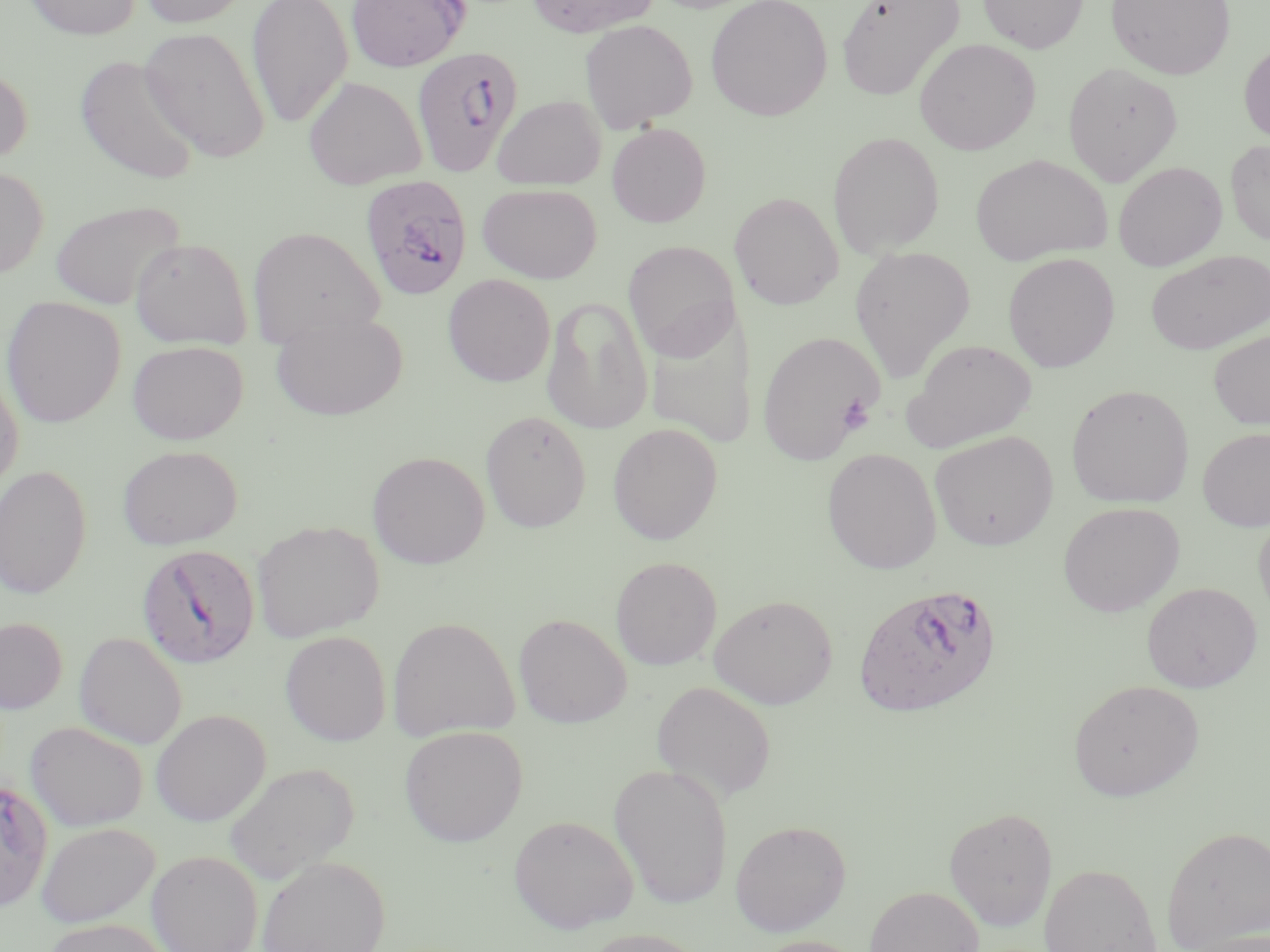

Approximate bounding boxes as (x1,y1)-(x2,y2) corner pairs in pixels. Uninfected red blood cell locations: (24,0)-(141,40), (136,0)-(254,29), (246,0)-(353,129), (346,0)-(469,72), (527,0)-(661,37), (835,0)-(965,101), (978,0)-(1088,53), (1106,0)-(1236,80), (705,1)-(833,121), (579,19)-(698,133), (139,26)-(271,163), (914,38)-(1040,155), (1239,42)-(1270,145), (74,54)-(201,185), (1063,61)-(1183,186), (0,64)-(33,168), (303,76)-(427,189), (492,94)-(606,191), (607,123)-(711,227), (828,131)-(945,258), (1225,139)-(1270,246), (969,153)-(1112,266), (1112,161)-(1227,271), (0,166)-(49,278), (477,183)-(602,284), (730,192)-(844,310), (49,199)-(185,310), (247,225)-(384,350), (130,237)-(253,349), (623,241)-(740,361), (849,245)-(976,381), (1146,250)-(1270,354), (1002,253)-(1120,372), (443,274)-(555,387), (1,295)-(126,427), (541,295)-(653,434), (643,305)-(757,448), (270,310)-(408,421), (757,330)-(883,465), (1208,330)-(1270,430), (901,338)-(1037,452), (127,340)-(248,445), (0,367)-(23,492), (1066,383)-(1195,508), (480,410)-(592,533), (607,423)-(724,544), (1198,426)-(1270,531), (929,430)-(1059,551), (117,444)-(243,550), (822,447)-(942,574), (367,451)-(489,569), (0,465)-(92,599), (1058,502)-(1185,617), (1254,510)-(1270,626), (251,520)-(385,642), (610,556)-(722,670), (1142,582)-(1261,692), (709,595)-(839,709), (513,613)-(632,728), (0,616)-(68,714), (387,616)-(519,742), (279,630)-(392,746), (74,632)-(187,749), (1068,679)-(1204,801), (652,681)-(777,802), (150,709)-(270,826), (25,721)-(148,832), (400,725)-(528,846), (223,761)-(359,883), (609,762)-(734,910), (0,775)-(54,914), (943,806)-(1058,930), (509,815)-(638,933), (729,819)-(851,936), (36,821)-(160,928), (1161,825)-(1270,951), (146,850)-(263,952), (257,856)-(389,952), (1039,862)-(1164,952), (865,885)-(985,952), (43,918)-(171,952), (579,928)-(710,952), (748,935)-(868,952). Platelet locations: (838,395)-(874,434). Plasmodium falciparum-infected red blood cell locations: (410,46)-(523,178), (359,174)-(473,301), (136,544)-(260,668), (853,582)-(1003,718). Slide-level diagnosis: Plasmodium falciparum. Captured at 1000x magnification. Thin blood film. Light microscopy. May-Grünwald-Giemsa-stained preparation. One field of a larger specimen. Image is 1270×952 pixels.